Assess this cell for malaria.
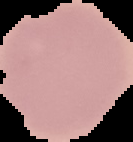
It is uninfected.

Cell region segmented out of the field of view; the surrounding area is masked to black. From a thin blood smear. Image is 133×142 pixels.